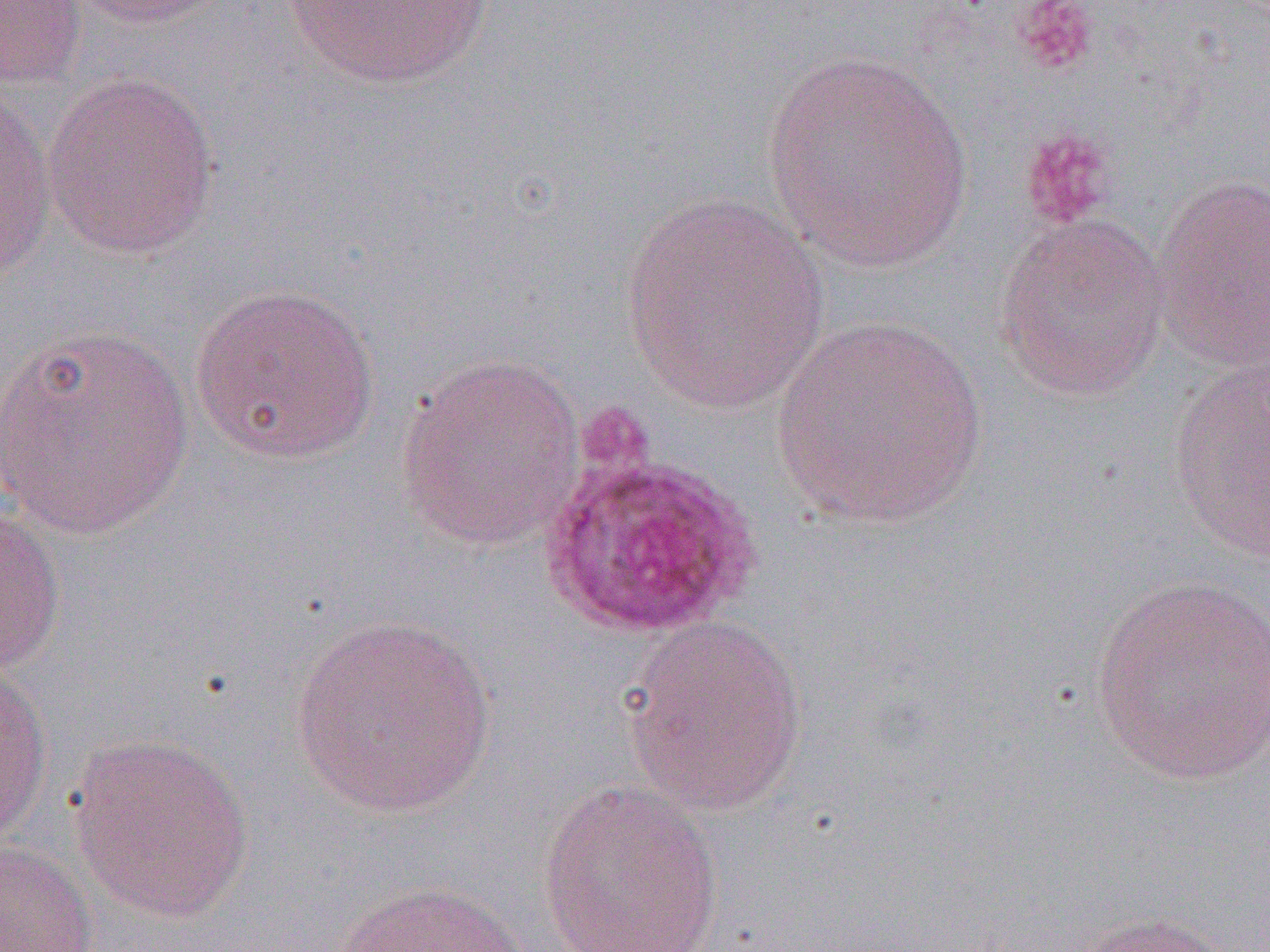 Approximate bounding boxes as named x1/y1/x2/y2 corners in pixels. Plasmodium ovale-infected red blood cell locations: (x1=537, y1=444, x2=763, y2=641). Platelet locations: (x1=1012, y1=1, x2=1100, y2=75), (x1=1019, y1=127, x2=1119, y2=233). Uninfected red blood cell locations: (x1=1, y1=0, x2=87, y2=90), (x1=65, y1=0, x2=231, y2=28), (x1=276, y1=0, x2=503, y2=92), (x1=759, y1=49, x2=976, y2=274), (x1=43, y1=69, x2=221, y2=261), (x1=0, y1=85, x2=58, y2=284), (x1=1152, y1=172, x2=1270, y2=373), (x1=617, y1=193, x2=830, y2=414), (x1=994, y1=212, x2=1171, y2=402), (x1=188, y1=281, x2=381, y2=465), (x1=770, y1=316, x2=992, y2=531), (x1=0, y1=321, x2=197, y2=541), (x1=394, y1=354, x2=586, y2=553), (x1=1169, y1=361, x2=1270, y2=560), (x1=0, y1=499, x2=66, y2=680), (x1=1090, y1=575, x2=1270, y2=788), (x1=287, y1=613, x2=499, y2=820), (x1=622, y1=616, x2=809, y2=819), (x1=0, y1=658, x2=53, y2=847), (x1=67, y1=733, x2=256, y2=926), (x1=536, y1=779, x2=725, y2=952), (x1=0, y1=840, x2=98, y2=951), (x1=330, y1=879, x2=536, y2=952), (x1=1072, y1=910, x2=1242, y2=952). Slide-level diagnosis: Plasmodium ovale. Thin blood film. Single field of view. Light microscopy. Image is 1270×952 pixels. 1000x magnification.